Give the position of every leukocyte visible.
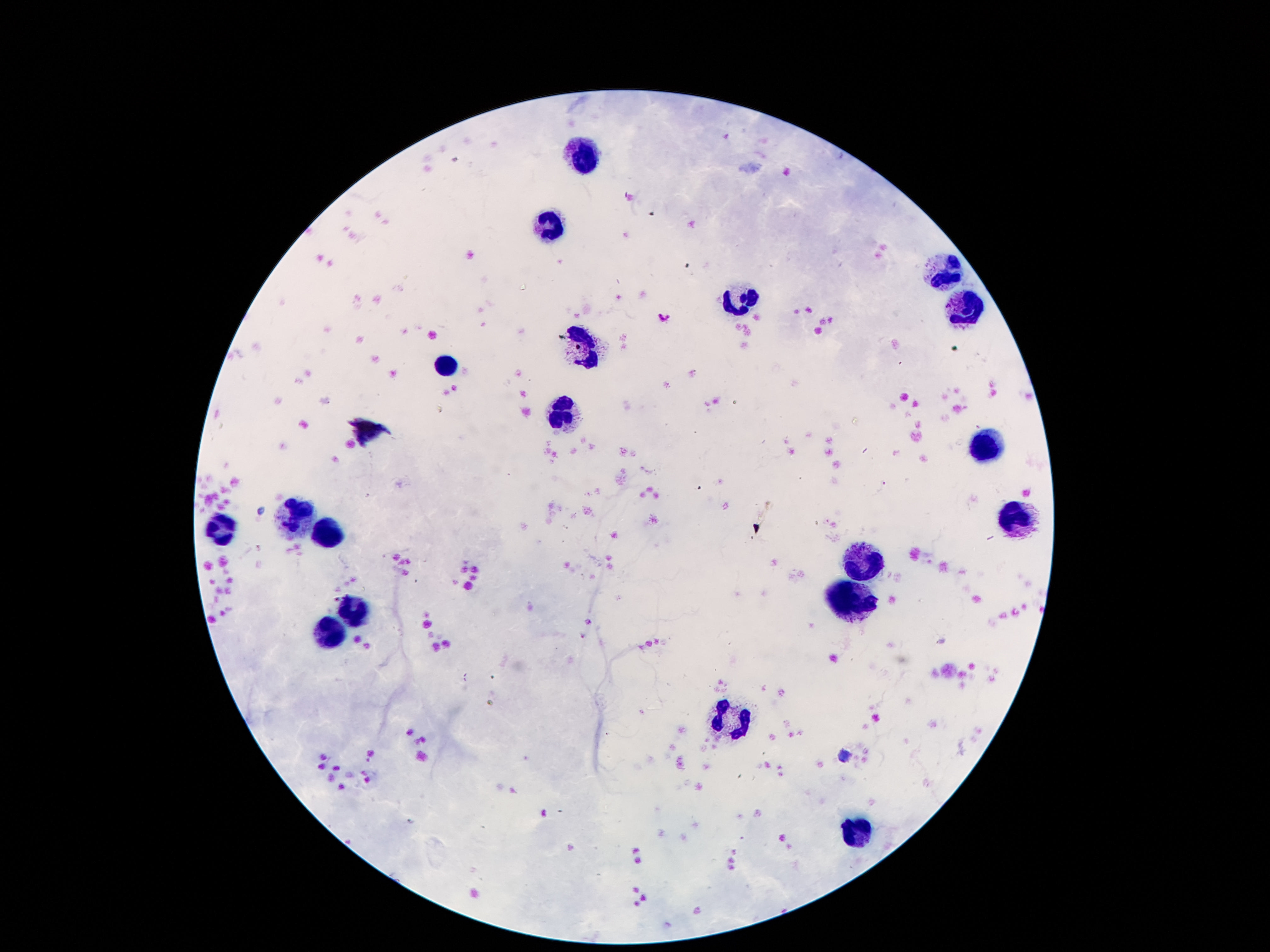
Approximate centers as {x, y} in pixels.
Leukocytes: {584, 160}, {550, 226}, {941, 274}, {739, 298}, {964, 308}, {587, 347}, {453, 362}, {564, 415}, {980, 443}, {298, 515}, {1018, 517}, {223, 530}, {328, 534}, {866, 566}, {848, 603}, {353, 607}, {330, 634}, {727, 717}, {861, 837}.

Patient malaria status: negative. One field from this slide. Image is 1270×952 pixels. Giemsa-stained preparation. Thick blood film. Photographed through the microscope eyepiece with a smartphone camera. 100x magnification.